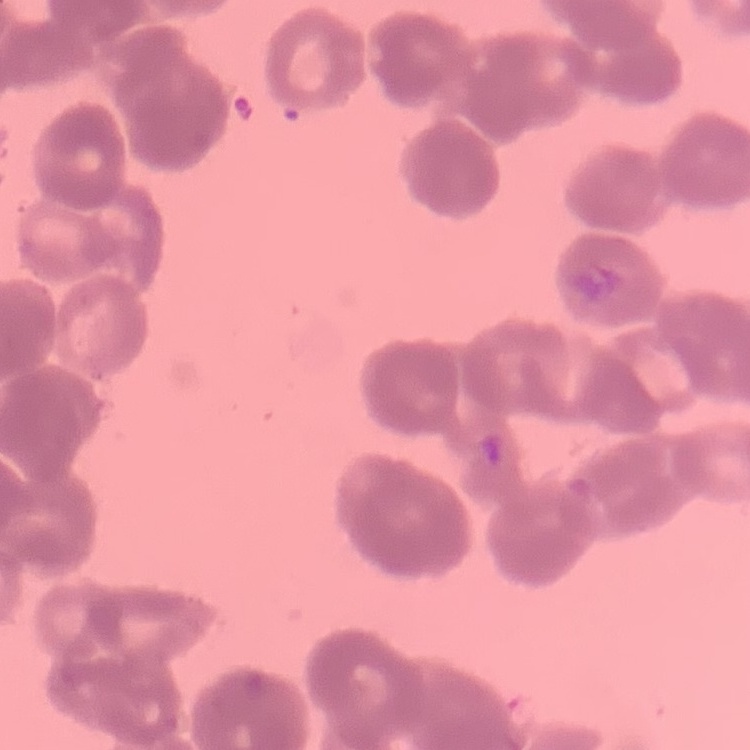
The red blood cells exhibit rouleaux formation. One tile cut from a larger photomicrograph. Field's or Giemsa stain. Thin blood film.